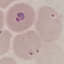
Result: malaria parasites identified. Photographed with a smartphone camera at the microscope eyepiece. Thin smear of blood. Giemsa-stained preparation. Automatically extracted cell patch, resized to 64 × 64 pixels.